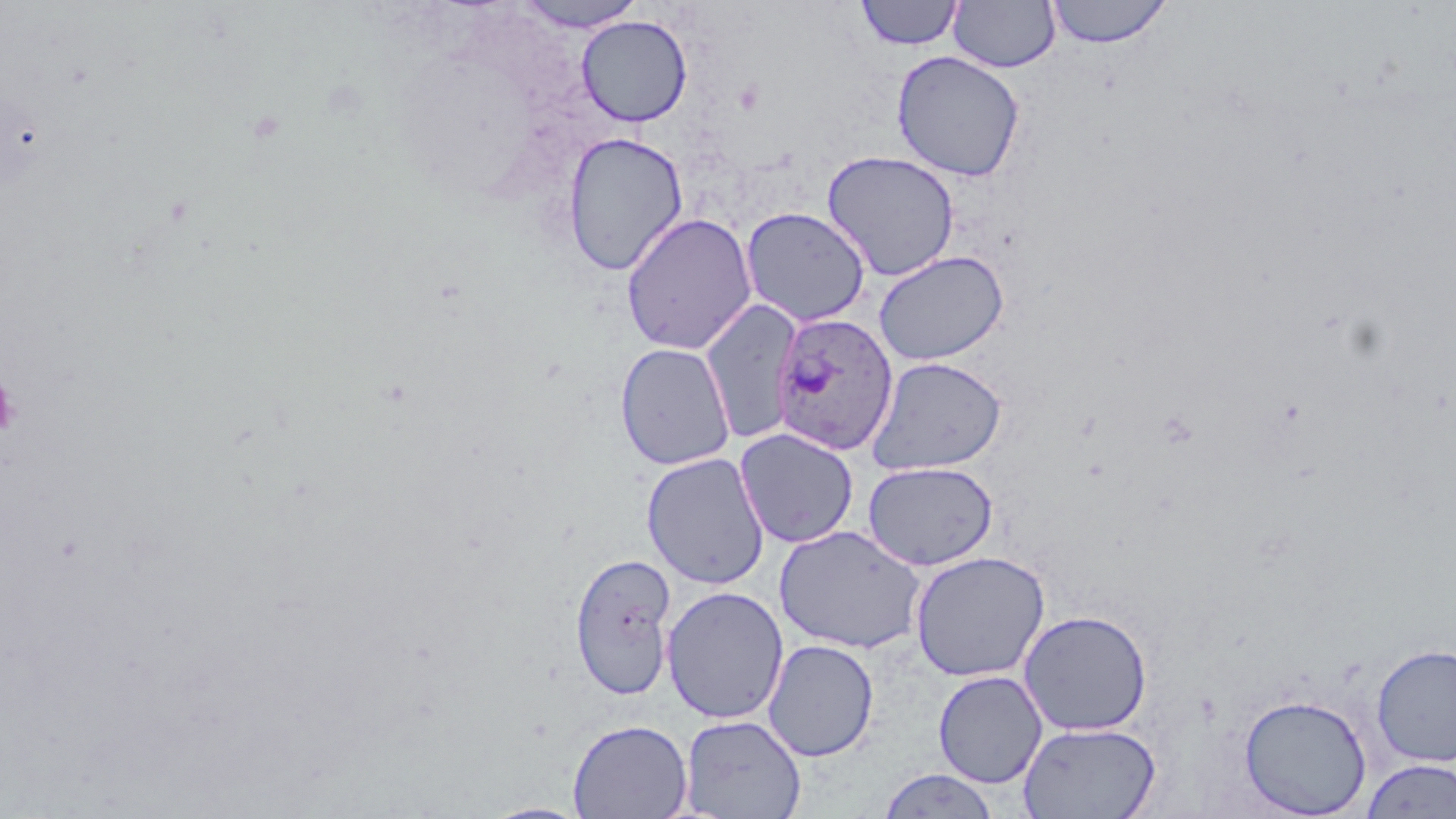
{
  "plasmodium_ovale_infected_red_blood_cell_locations": "approximate bounding boxes as (x1, y1, x2, y2) in pixels: (770, 312, 899, 455)",
  "slide_level_diagnosis": "Plasmodium ovale",
  "field_of_view": "single",
  "preparation": "thin blood smear",
  "image_size": "1456×819 pixels",
  "magnification": "1000x",
  "modality": "light microscopy",
  "platelet_locations": "approximate bounding boxes as (x1, y1, x2, y2) in pixels: (0, 376, 20, 439)",
  "uninfected_red_blood_cell_locations": "approximate bounding boxes as (x1, y1, x2, y2) in pixels: (512, 0, 649, 32), (948, 0, 1060, 73), (1046, 0, 1172, 48), (854, 1, 965, 51), (576, 15, 692, 127), (891, 50, 1025, 182), (561, 132, 688, 276), (822, 150, 960, 282), (740, 206, 871, 327), (621, 212, 757, 354), (873, 250, 1010, 365), (701, 298, 802, 444), (615, 342, 736, 471), (867, 356, 1007, 475), (734, 427, 859, 548), (641, 452, 770, 590), (862, 460, 999, 570), (774, 525, 926, 653), (910, 550, 1050, 682), (569, 551, 678, 700), (661, 586, 789, 724), (1018, 609, 1153, 736), (763, 639, 879, 761), (1371, 643, 1456, 766), (933, 670, 1048, 788), (1238, 693, 1372, 817), (679, 714, 806, 819), (568, 718, 692, 819), (1018, 721, 1161, 819), (1359, 758, 1456, 818), (876, 768, 1001, 818), (480, 801, 592, 819)",
  "stain": "May-Grünwald-Giemsa"
}